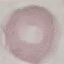 Malaria status: uninfected. Giemsa-stained preparation. Photographed with a smartphone camera at the microscope eyepiece. Automatically extracted cell patch, resized to 64 × 64 pixels. Thin blood smear.